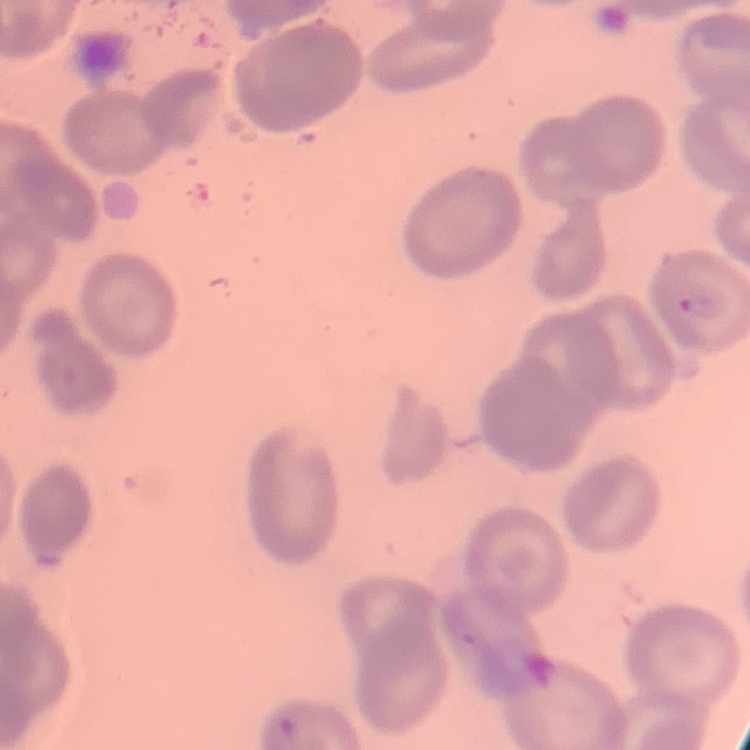
Summary:
  - Red blood cell morphology: no rouleaux formation
  - Preparation: thin peripheral smear
  - Image type: one tile cut from a larger photomicrograph
  - Stain: Field's or Giemsa